State which cell type is depicted.
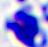
This is a leukocyte.

Summary:
  - Modality: photomicrograph
  - Magnification: 400x